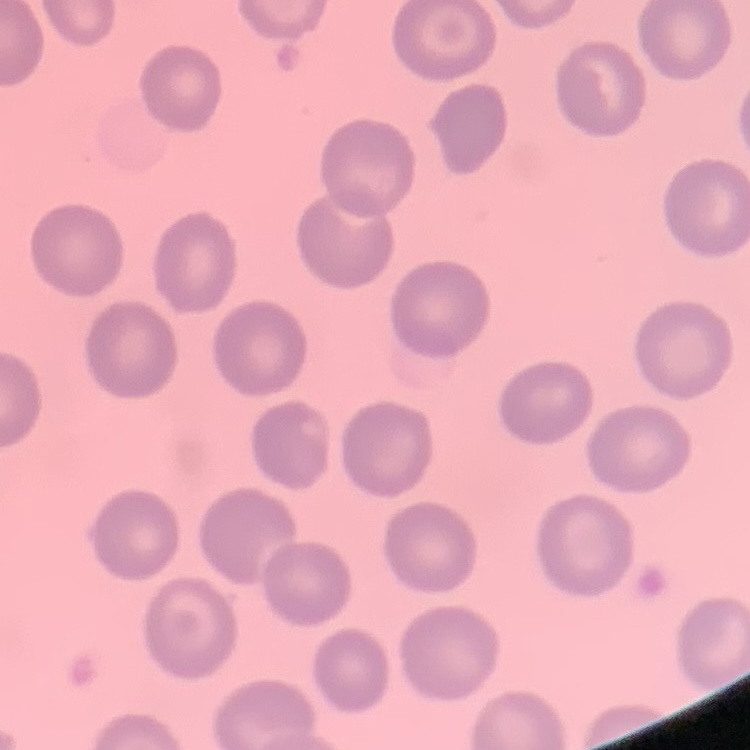
erythrocyte morphology = no rouleaux formation
stain = Field's or Giemsa
image type = one tile cut from a larger photomicrograph
preparation = thin peripheral smear